Identify the parasite.
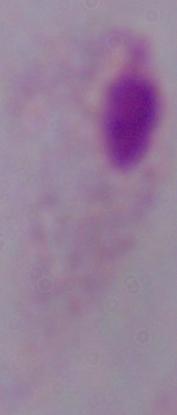
A trichomonad.

Photomicrograph. 1000x magnification.